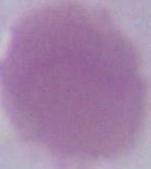
An erythrocyte is shown. Captured at 1000x magnification. Micrograph.